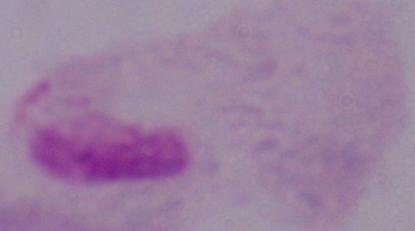

modality: photomicrograph
identification: trichomonad
magnification: 1000x